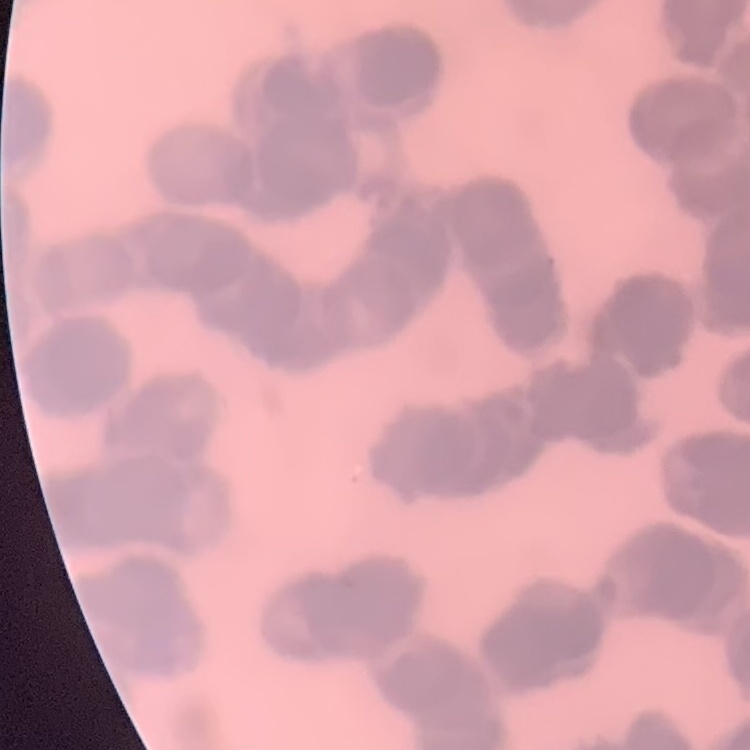
The erythrocytes exhibit rouleaux formation. Field's or Giemsa stain. Thin blood smear. Square crop of a larger photomicrograph.